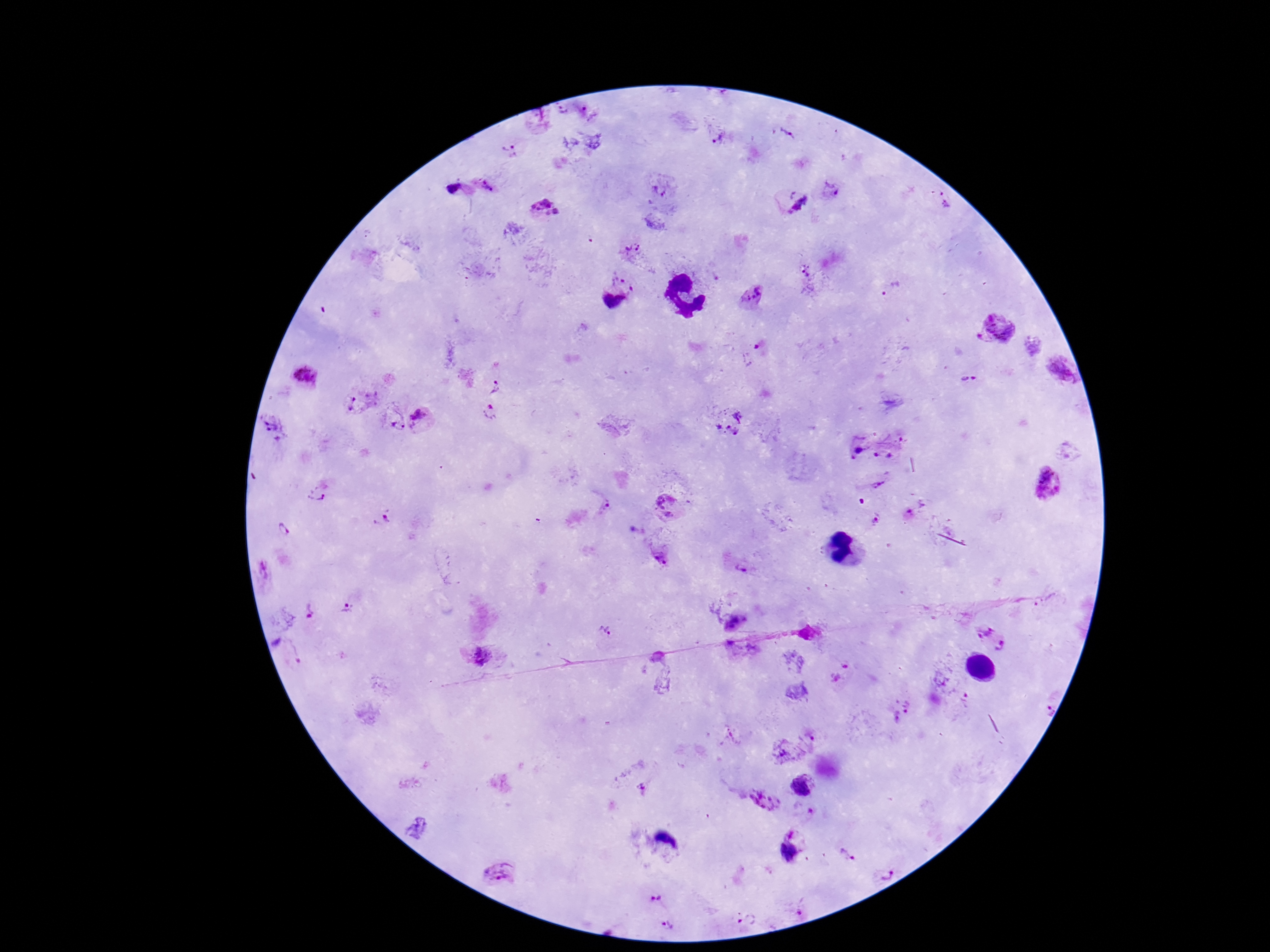
{
  "stain": "Giemsa",
  "plasmodium_parasite_locations": "approximate centers as [x, y] in pixels: [563, 108], [786, 136], [719, 139], [512, 150], [490, 183], [454, 187], [658, 190], [829, 191], [945, 200], [792, 201], [546, 208], [632, 250], [806, 271], [626, 278], [892, 289], [752, 297], [613, 303], [998, 327], [1060, 371], [304, 376], [967, 379], [495, 386], [362, 403], [490, 412], [423, 420], [728, 422], [395, 424], [273, 429], [903, 439], [855, 449], [884, 452], [1046, 484], [877, 485], [319, 491], [666, 505], [914, 506], [606, 507], [874, 518], [383, 519], [283, 530], [659, 558], [739, 568], [347, 609], [308, 612], [736, 620], [604, 632], [993, 639], [293, 651], [480, 655], [963, 699], [1047, 703], [901, 709], [811, 740], [782, 751], [643, 784], [804, 785], [764, 801], [789, 853], [847, 855], [884, 871], [498, 872], [656, 897], [801, 913], [747, 918], [667, 925]",
  "field_of_view": "one from this slide",
  "image_size": "1270×952 pixels",
  "capture": "smartphone camera through the microscope eyepiece",
  "magnification": "100x",
  "preparation": "thick blood smear",
  "patient_malaria_status": "positive"
}